Point out Plasmodium parasites and leukocytes.
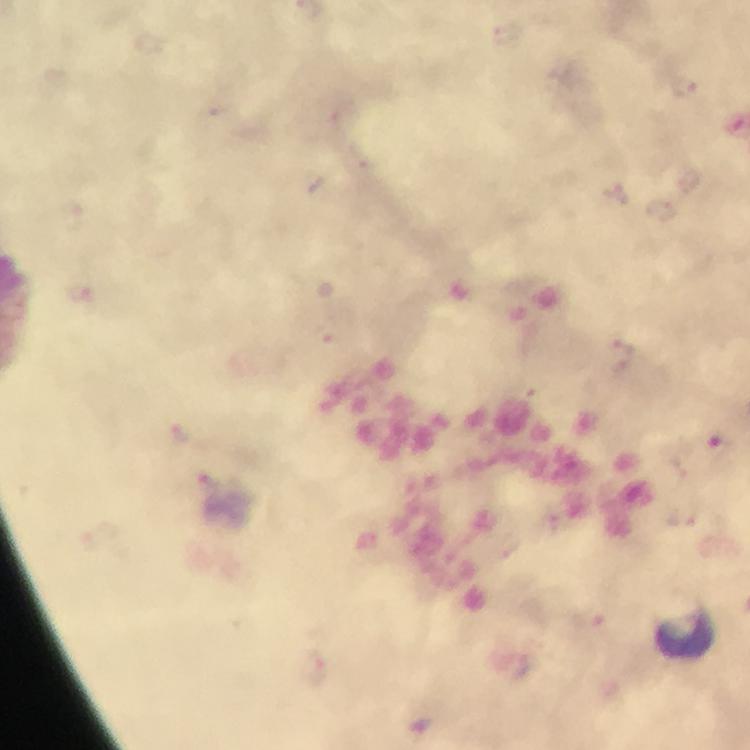
Approximate object centers, in pixels from the top-left corner.
Plasmodium parasites: (x=720, y=451).
Leukocytes: (x=684, y=635).

100x magnification. Immersion oil applied. Thick blood smear. Cropped region of a single field of view. From a malaria diagnostic workup. Smartphone photograph taken through a microscope. Giemsa stain. Image is 750×750 pixels.